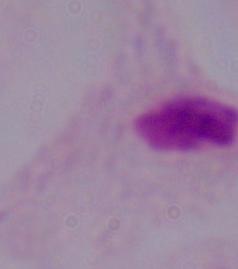
A trichomonad is shown. Photomicrograph. Captured at 1000x magnification.